Locate every blood parasite and identify its species.
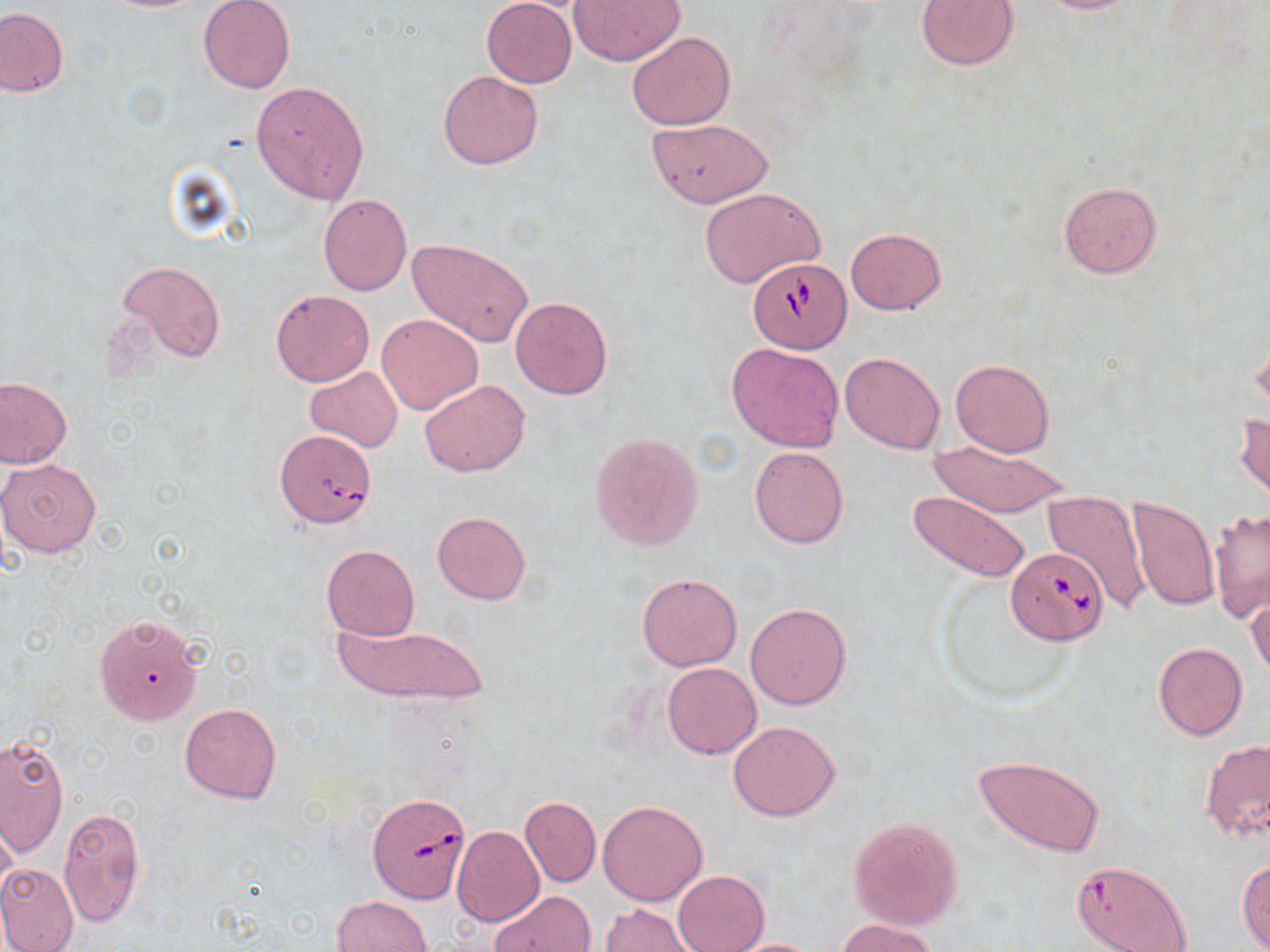
Approximate bounding boxes as (x1, y1, x2, y2) in pixels.
Babesia divergens-infected red blood cells: (747, 257, 850, 353), (275, 429, 377, 528), (1006, 548, 1106, 644), (369, 794, 472, 903).
No Plasmodium falciparum, Plasmodium ovale, Plasmodium malariae, Plasmodium vivax, or Trypanosoma brucei observed.

slide_level_diagnosis: Babesia divergens
magnification: 1000x
image_size: 1270×952 pixels
modality: light microscopy
stain: May-Grünwald-Giemsa
field_of_view: one of a larger specimen
uninfected_red_blood_cell_locations: 'approximate bounding boxes as (x1, y1, x2, y2) in pixels: (198, 0, 295, 93), (481, 0, 576, 87), (568, 0, 686, 67), (915, 0, 1020, 71), (1032, 0, 1143, 14), (462, 6, 566, 153), (0, 8, 69, 97), (628, 31, 735, 131), (437, 71, 542, 170), (250, 81, 369, 204), (646, 118, 772, 207), (1058, 180, 1163, 279), (700, 188, 825, 287), (317, 194, 413, 296), (844, 228, 946, 316), (408, 237, 533, 346), (119, 259, 226, 362), (271, 290, 374, 387), (510, 298, 613, 399), (378, 314, 483, 414), (1248, 331, 1269, 417), (727, 343, 844, 452), (840, 351, 945, 454), (950, 359, 1054, 457), (303, 366, 405, 453), (0, 377, 72, 469), (419, 379, 530, 477), (1233, 410, 1269, 508), (589, 432, 704, 551), (926, 442, 1071, 517), (748, 446, 849, 548), (0, 457, 102, 557), (908, 491, 1031, 583), (1043, 491, 1150, 611), (1125, 495, 1219, 612), (1209, 506, 1270, 623), (432, 511, 530, 605), (321, 544, 420, 640), (637, 572, 743, 671), (1247, 586, 1270, 682), (745, 602, 852, 711), (94, 613, 204, 724), (335, 622, 488, 704), (1152, 642, 1249, 741), (662, 662, 761, 758), (179, 702, 282, 804), (727, 721, 840, 821), (0, 734, 69, 856), (1200, 738, 1270, 843), (973, 753, 1104, 856), (519, 796, 601, 887), (598, 800, 708, 906), (59, 806, 147, 929), (0, 816, 19, 908), (849, 817, 962, 930), (452, 827, 545, 927), (1237, 859, 1270, 951), (1072, 860, 1191, 951), (0, 861, 79, 952), (672, 870, 769, 952), (492, 889, 594, 952), (331, 895, 433, 952), (600, 902, 698, 952), (837, 918, 940, 952), (725, 938, 825, 951)'
preparation: thin blood smear